Locate every blood parasite and identify its species.
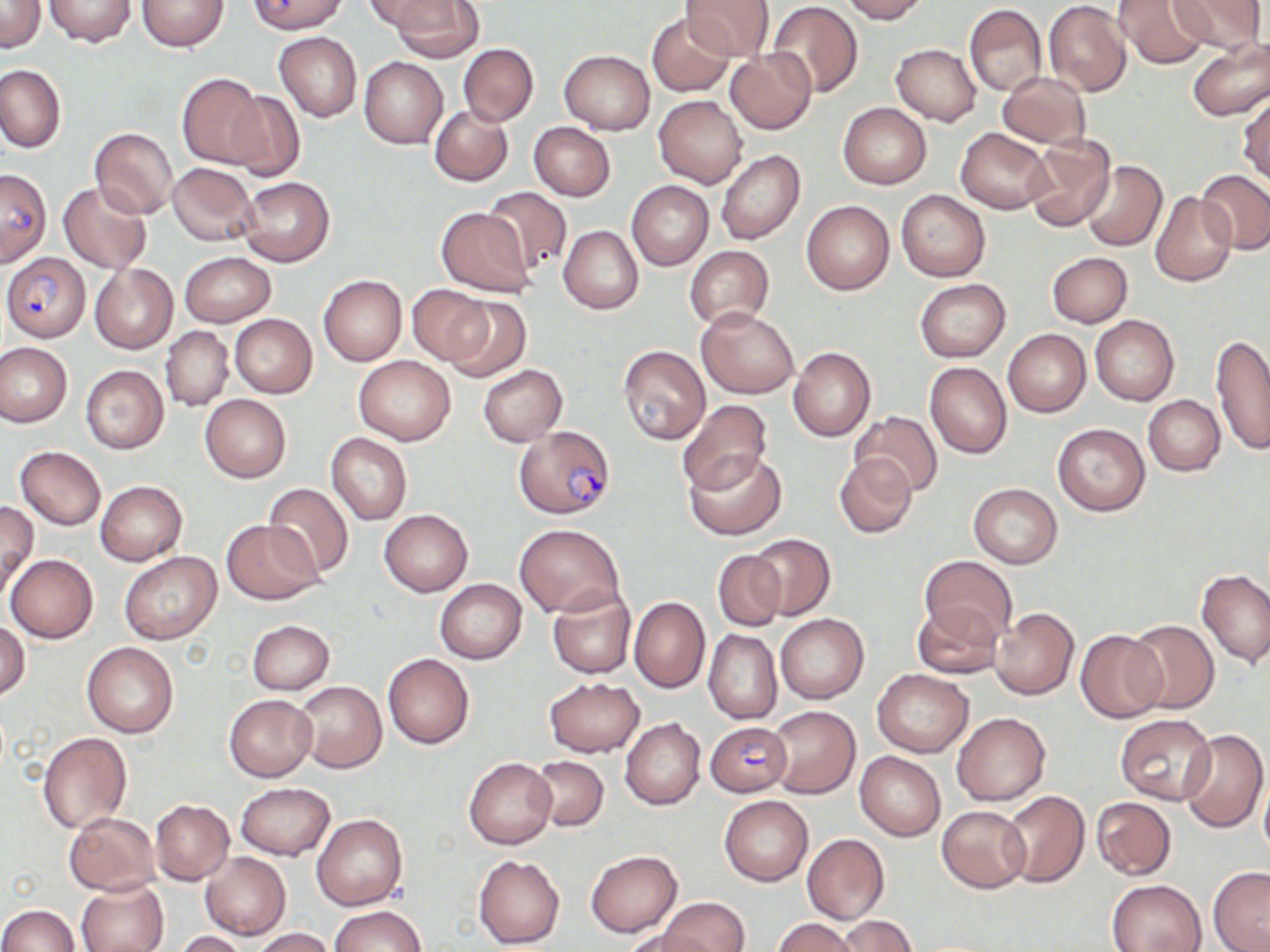

Approximate bounding boxes as (x1,y1)-(x2,y2) corner pairs in pixels.
Plasmodium falciparum-infected red blood cells: (0,169)-(52,269), (3,254)-(91,342), (515,424)-(614,518), (704,719)-(790,795).
No Plasmodium ovale, Plasmodium malariae, Plasmodium vivax, Babesia divergens, or Trypanosoma brucei observed.

{
  "slide_level_diagnosis": "Plasmodium falciparum",
  "preparation": "thin blood smear",
  "field_of_view": "single",
  "modality": "optical microscopy",
  "magnification": "1000x",
  "image_size": "1270×952 pixels",
  "uninfected_red_blood_cell_locations": "approximate bounding boxes as (x1,y1)-(x2,y2) corner pairs in pixels: (0,0)-(45,53), (136,0)-(229,51), (362,0)-(453,36), (385,0)-(482,61), (681,0)-(773,62), (839,0)-(928,23), (1113,0)-(1209,69), (1170,0)-(1264,56), (44,1)-(137,47), (248,1)-(347,34), (768,2)-(862,99), (1043,2)-(1130,97), (964,4)-(1047,97), (646,13)-(735,96), (275,32)-(362,120), (1186,38)-(1270,122), (457,43)-(538,127), (891,44)-(982,126), (725,49)-(816,135), (560,50)-(654,134), (359,57)-(447,148), (0,64)-(65,152), (998,72)-(1090,149), (177,74)-(269,168), (222,89)-(306,182), (1237,92)-(1269,185), (653,95)-(748,188), (838,104)-(931,189), (430,105)-(513,186), (529,122)-(615,202), (90,127)-(178,218), (956,127)-(1053,214), (1022,137)-(1116,233), (716,149)-(804,244), (1081,161)-(1166,251), (168,163)-(258,246), (1196,169)-(1269,256), (237,176)-(334,266), (627,180)-(712,271), (58,181)-(152,273), (483,186)-(571,275), (896,189)-(990,281), (1150,193)-(1236,285), (801,200)-(895,295), (435,207)-(536,296), (559,226)-(643,314), (686,245)-(775,331), (179,252)-(275,327), (1047,252)-(1132,327), (89,263)-(178,353), (318,275)-(407,365), (915,279)-(1010,361), (408,285)-(491,364), (442,296)-(531,383), (696,306)-(798,398), (230,314)-(317,398), (1090,314)-(1179,406), (161,327)-(233,412), (1002,329)-(1091,417), (1211,334)-(1270,455), (0,342)-(72,427), (618,344)-(710,444), (787,347)-(875,441), (355,356)-(456,445), (925,362)-(1012,459), (80,365)-(169,454), (477,365)-(566,446), (199,394)-(292,482), (1143,395)-(1226,476), (678,399)-(773,494), (850,411)-(944,498), (1052,423)-(1150,516), (325,433)-(411,526), (15,446)-(106,529), (684,448)-(788,541), (834,454)-(918,538), (95,481)-(187,565), (263,482)-(354,578), (969,483)-(1061,567), (0,502)-(38,597), (379,510)-(473,596), (221,519)-(323,604), (515,524)-(623,617), (748,532)-(836,621), (712,550)-(787,631), (120,552)-(219,645), (7,554)-(98,643), (921,556)-(1016,643), (1197,568)-(1270,666), (435,579)-(527,664), (547,588)-(636,679), (629,597)-(709,693), (911,601)-(1005,681), (991,608)-(1079,699), (774,614)-(869,703), (0,618)-(30,701), (247,620)-(334,695), (1124,620)-(1218,714), (703,629)-(781,724), (1076,629)-(1166,722), (82,643)-(179,738), (383,653)-(474,748), (872,669)-(973,757), (543,676)-(644,757), (294,680)-(387,773), (224,693)-(318,782), (766,705)-(860,798), (951,713)-(1051,805), (1115,715)-(1217,804), (621,718)-(706,810), (1179,728)-(1268,832), (37,732)-(131,833), (855,752)-(945,840), (529,756)-(608,830), (464,758)-(556,849), (1260,773)-(1270,864), (235,783)-(334,860), (1000,790)-(1090,888), (719,795)-(813,886), (1091,796)-(1177,880), (150,800)-(233,884), (936,805)-(1031,893), (64,811)-(161,895), (312,814)-(407,910), (802,834)-(889,924), (585,849)-(682,936), (200,852)-(290,939), (474,854)-(565,948), (1207,867)-(1270,952), (1108,879)-(1205,952), (76,881)-(168,952), (659,898)-(750,952), (0,905)-(80,951), (332,905)-(424,952), (838,915)-(917,952), (772,918)-(860,952), (251,928)-(334,952), (621,929)-(719,952), (173,931)-(250,952)",
  "stain": "May-Grünwald-Giemsa"
}